Assess the morphology of the red blood cells.
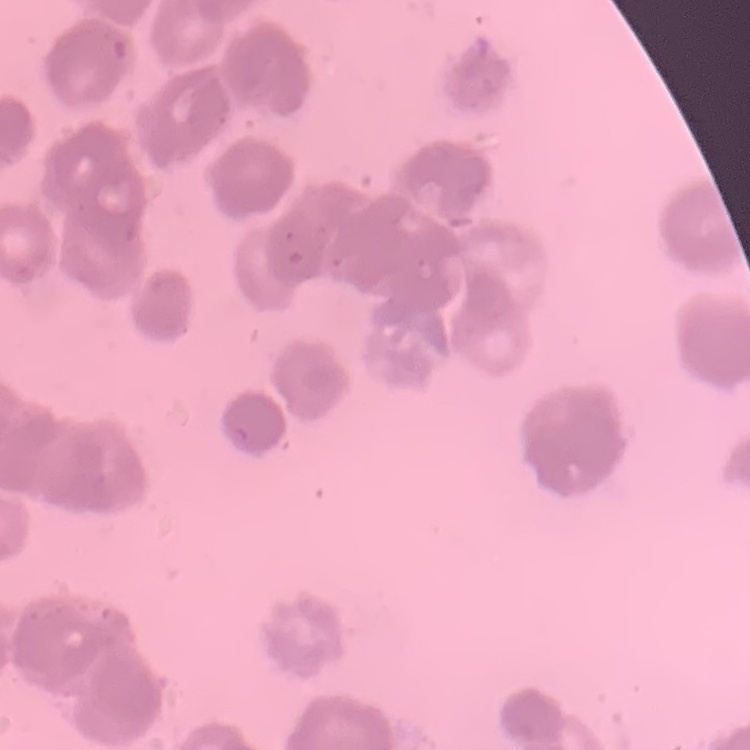

Rouleaux formation.

Summary:
  - Image type: one tile cut from a larger photomicrograph
  - Stain: Field's or Giemsa
  - Preparation: thin peripheral smear